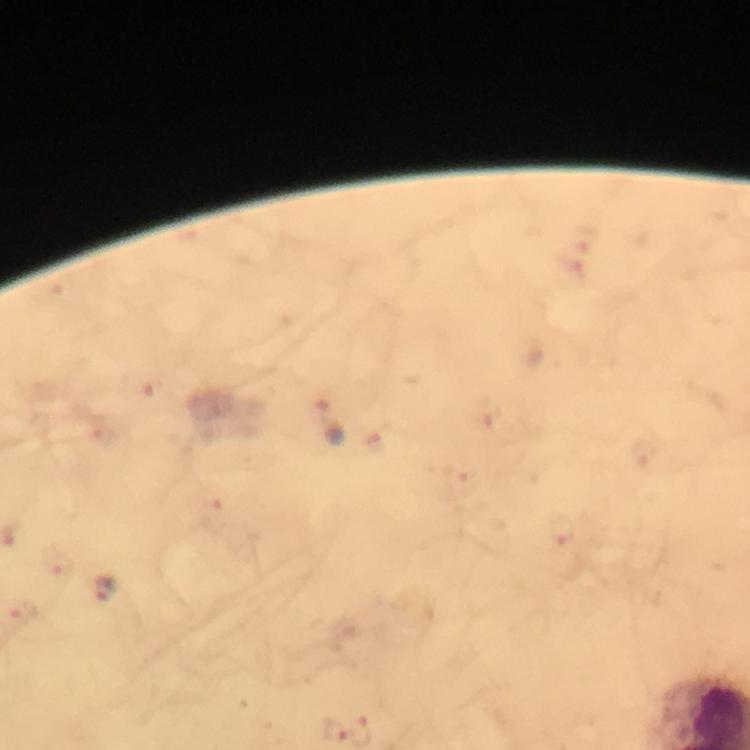
Approximate centers as [x, y] in pixels.
Summary:
  - Plasmodium parasite locations: [329, 420], [60, 562], [106, 591], [23, 611]
  - Capture: smartphone camera through the microscope
  - Context: from a diagnostic examination for malaria
  - Image size: 750×750 pixels
  - Stain: Giemsa
  - Immersion oil: applied
  - Cropped from: a single field of view
  - Preparation: thick blood film
  - Magnification: 100x